Locate every Plasmodium parasite.
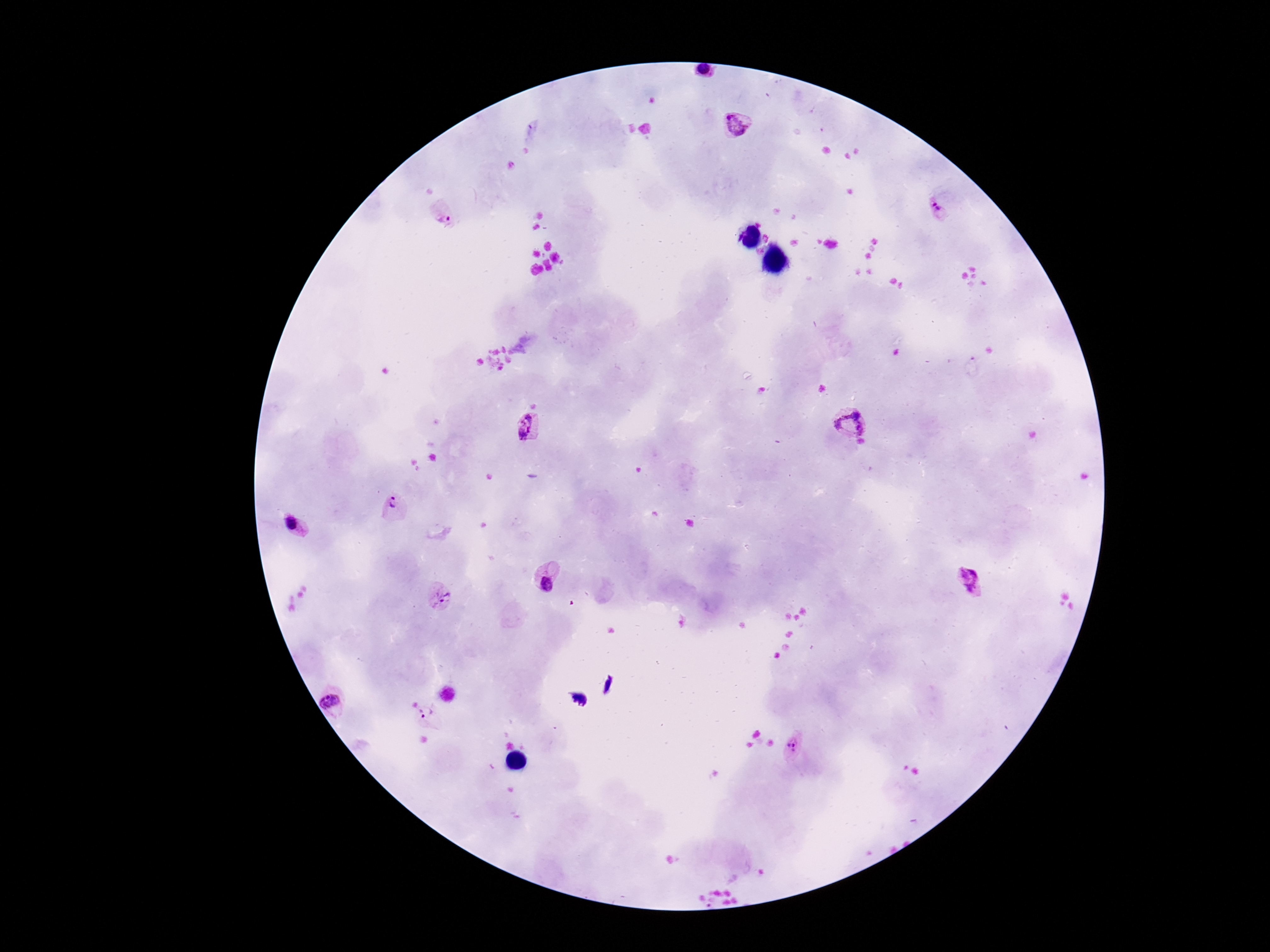

Approximate centers as [x, y] in pixels.
Plasmodium parasites: [703, 72], [736, 124], [939, 206], [445, 214], [852, 425], [532, 428], [394, 508], [295, 530], [547, 579], [969, 582], [442, 597], [332, 704], [427, 715], [796, 745].

Giemsa stain. Patient malaria status: positive. Image is 1270×952 pixels. Photographed through the microscope eyepiece with a smartphone camera. Thick peripheral-blood smear. One field from this slide. 100x magnification.